State the preparation type.
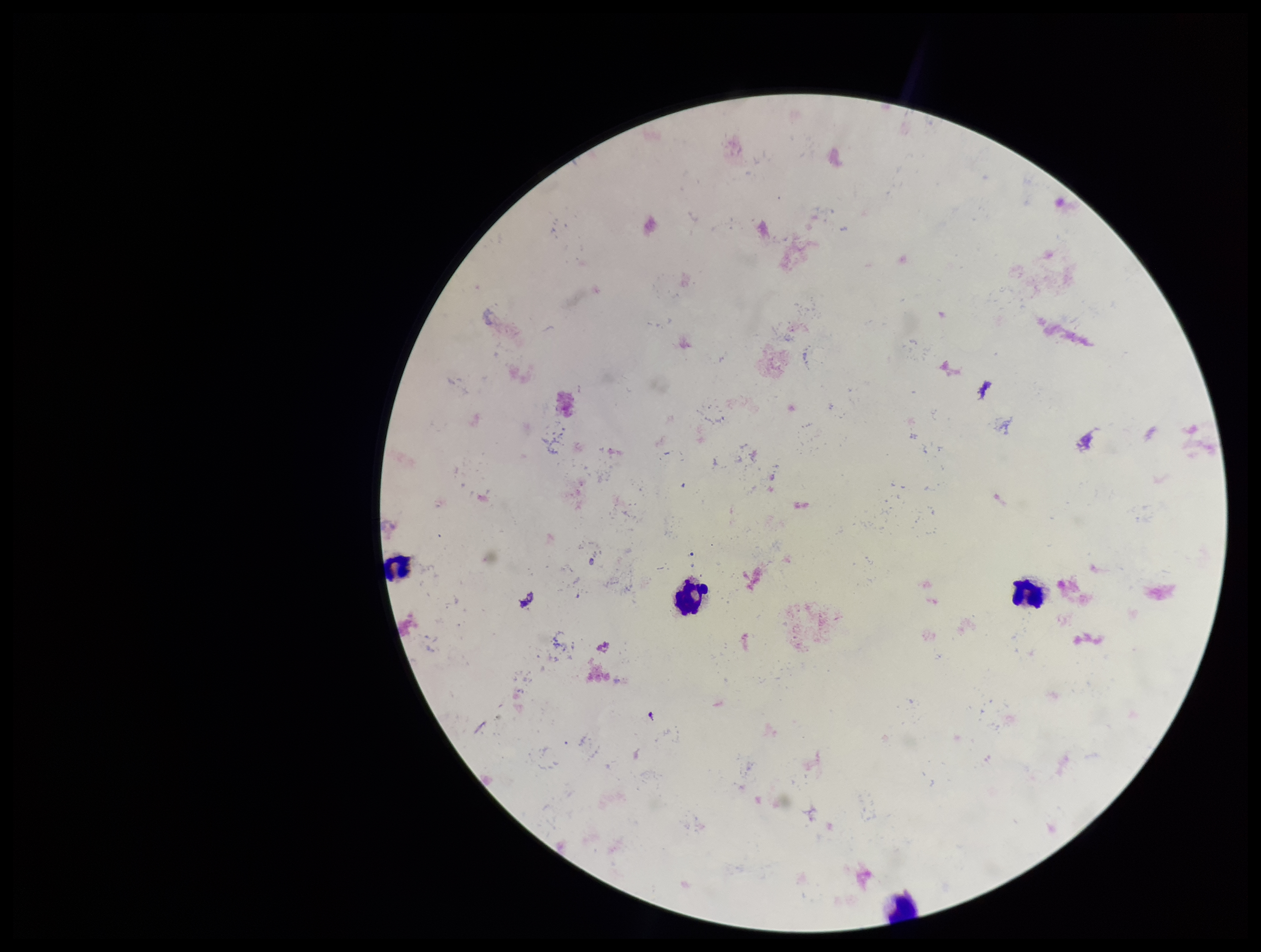

It is a thick blood smear.

Single field of view. Giemsa stain. Smartphone photograph taken through the eyepiece of a microscope. Image is 1261×952 pixels. Plasmodium parasites: none detected. Patient malaria status: negative. Parasite count: 0. Leukocyte count: 4.